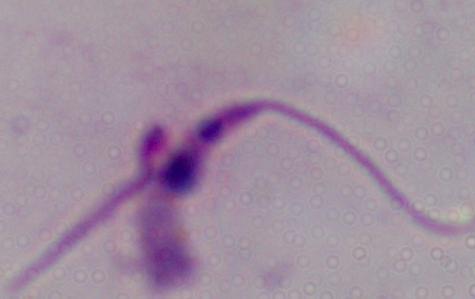

{
  "modality": "photomicrograph",
  "identification": "Leishmania",
  "magnification": "1000x"
}